Assess this cell for malaria.
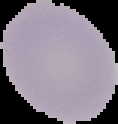

It is uninfected.

Summary:
  - Image size: 118×124 pixels
  - Preparation: thin blood film
  - Image type: cell region segmented out of the field of view; surrounding area masked to black